State which parasite is depicted.
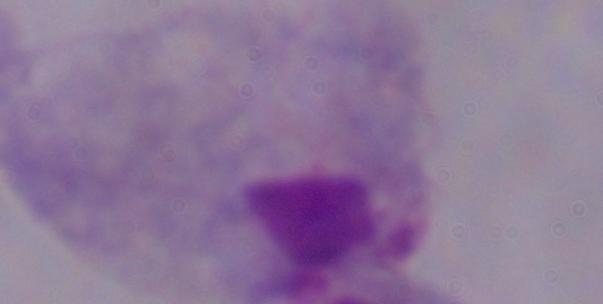

This is a trichomonad.

Summary:
  - Magnification: 1000x
  - Modality: photomicrograph